Outline each uninfected red blood cell.
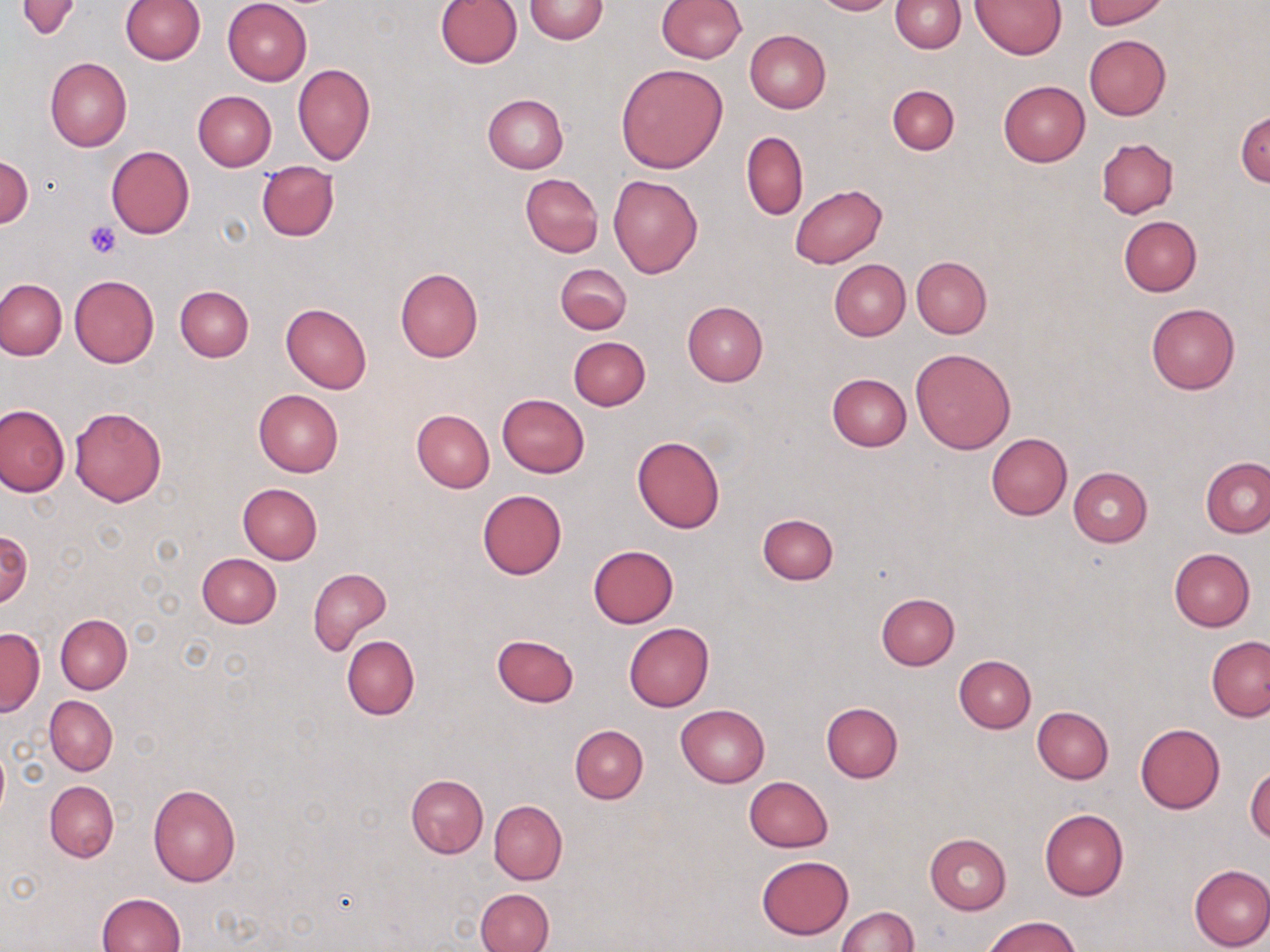
Approximate bounding boxes as named x1/y1/x2/y2 corners in pixels.
Uninfected red blood cells: (x1=15, y1=0, x2=83, y2=40), (x1=435, y1=0, x2=521, y2=69), (x1=656, y1=0, x2=747, y2=63), (x1=810, y1=0, x2=896, y2=15), (x1=892, y1=0, x2=964, y2=52), (x1=971, y1=0, x2=1066, y2=59), (x1=1082, y1=0, x2=1167, y2=28), (x1=120, y1=1, x2=205, y2=65), (x1=222, y1=1, x2=312, y2=85), (x1=524, y1=1, x2=608, y2=43), (x1=744, y1=30, x2=831, y2=113), (x1=1084, y1=35, x2=1171, y2=119), (x1=45, y1=57, x2=133, y2=152), (x1=615, y1=62, x2=729, y2=174), (x1=292, y1=63, x2=376, y2=165), (x1=998, y1=81, x2=1090, y2=166), (x1=887, y1=84, x2=960, y2=155), (x1=193, y1=91, x2=277, y2=170), (x1=483, y1=93, x2=568, y2=174), (x1=1236, y1=107, x2=1270, y2=187), (x1=741, y1=131, x2=808, y2=221), (x1=1097, y1=138, x2=1178, y2=218), (x1=106, y1=145, x2=195, y2=240), (x1=1, y1=155, x2=32, y2=229), (x1=255, y1=162, x2=340, y2=242), (x1=519, y1=173, x2=604, y2=257), (x1=609, y1=175, x2=702, y2=278), (x1=790, y1=184, x2=887, y2=269), (x1=1119, y1=215, x2=1202, y2=295), (x1=911, y1=257, x2=992, y2=339), (x1=829, y1=259, x2=910, y2=341), (x1=556, y1=263, x2=631, y2=335), (x1=396, y1=268, x2=482, y2=362), (x1=69, y1=274, x2=159, y2=369), (x1=0, y1=279, x2=66, y2=359), (x1=175, y1=284, x2=254, y2=361), (x1=683, y1=302, x2=768, y2=385), (x1=281, y1=303, x2=371, y2=394), (x1=1146, y1=303, x2=1240, y2=394), (x1=567, y1=336, x2=651, y2=411), (x1=910, y1=348, x2=1015, y2=454), (x1=827, y1=373, x2=911, y2=451), (x1=253, y1=390, x2=343, y2=477), (x1=497, y1=394, x2=590, y2=477), (x1=1, y1=404, x2=68, y2=496), (x1=69, y1=407, x2=167, y2=507), (x1=412, y1=409, x2=495, y2=492), (x1=986, y1=433, x2=1072, y2=519), (x1=631, y1=435, x2=725, y2=533), (x1=1201, y1=457, x2=1270, y2=538), (x1=1068, y1=466, x2=1152, y2=547), (x1=237, y1=483, x2=323, y2=565), (x1=477, y1=490, x2=566, y2=579), (x1=757, y1=512, x2=839, y2=585), (x1=0, y1=528, x2=32, y2=608), (x1=589, y1=544, x2=678, y2=627), (x1=1169, y1=548, x2=1254, y2=631), (x1=197, y1=554, x2=282, y2=628), (x1=308, y1=567, x2=391, y2=654), (x1=876, y1=593, x2=958, y2=669), (x1=55, y1=615, x2=131, y2=693), (x1=624, y1=622, x2=714, y2=711), (x1=0, y1=628, x2=43, y2=716), (x1=492, y1=634, x2=579, y2=708), (x1=341, y1=635, x2=419, y2=720), (x1=1207, y1=635, x2=1270, y2=722), (x1=954, y1=655, x2=1036, y2=732), (x1=45, y1=695, x2=118, y2=775), (x1=821, y1=701, x2=903, y2=782), (x1=675, y1=704, x2=770, y2=788), (x1=1032, y1=706, x2=1113, y2=784), (x1=1134, y1=722, x2=1225, y2=814), (x1=570, y1=725, x2=648, y2=804), (x1=0, y1=744, x2=9, y2=819), (x1=1245, y1=764, x2=1270, y2=844), (x1=406, y1=774, x2=488, y2=857), (x1=743, y1=776, x2=834, y2=852), (x1=45, y1=781, x2=119, y2=862), (x1=148, y1=783, x2=241, y2=886), (x1=488, y1=800, x2=567, y2=885), (x1=1040, y1=808, x2=1128, y2=900), (x1=924, y1=833, x2=1012, y2=913), (x1=757, y1=855, x2=853, y2=940), (x1=1188, y1=864, x2=1270, y2=952), (x1=475, y1=888, x2=553, y2=952), (x1=98, y1=891, x2=186, y2=952), (x1=835, y1=906, x2=919, y2=951), (x1=982, y1=914, x2=1081, y2=952).

Platelet locations: (x1=85, y1=222, x2=120, y2=259). Slide-level diagnosis: no evidence of blood parasites. May-Grünwald-Giemsa stain. Captured at 1000x magnification. Thin blood film. One field of a larger specimen. Light microscopy. Image is 1270×952 pixels.